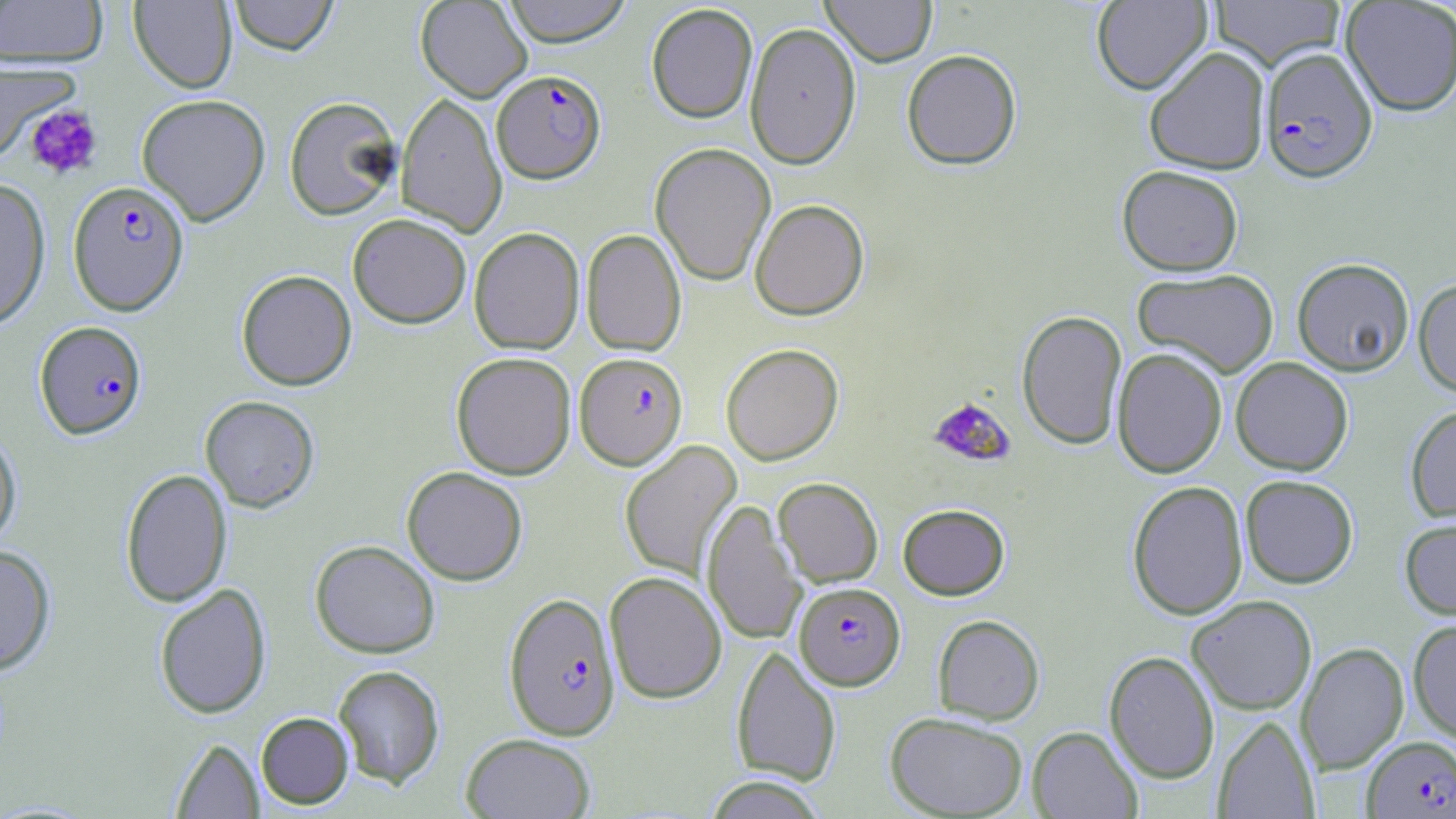
Approximate bounding boxes as (x1, y1, x2, y2) in pixels. Plasmodium falciparum-infected red blood cell locations: (1260, 47, 1378, 183), (492, 70, 606, 183), (67, 181, 189, 315), (34, 321, 147, 439), (577, 355, 690, 472), (795, 582, 905, 690), (503, 591, 621, 742), (1362, 735, 1456, 818). Uninfected red blood cell locations: (129, 0, 238, 94), (228, 0, 339, 56), (415, 0, 533, 102), (500, 0, 633, 46), (820, 0, 937, 67), (1091, 0, 1212, 95), (1341, 0, 1456, 116), (0, 1, 108, 68), (1210, 1, 1345, 71), (645, 3, 758, 124), (744, 22, 862, 169), (1143, 46, 1271, 175), (901, 50, 1022, 170), (0, 58, 80, 164), (395, 92, 507, 237), (136, 93, 271, 226), (284, 96, 402, 221), (650, 142, 776, 286), (1117, 165, 1243, 276), (0, 179, 51, 330), (750, 198, 869, 320), (348, 213, 472, 328), (468, 227, 585, 354), (581, 228, 686, 356), (1292, 257, 1414, 376), (1133, 268, 1279, 378), (236, 269, 357, 390), (1413, 277, 1456, 397), (1016, 309, 1127, 450), (720, 343, 844, 465), (1112, 347, 1228, 478), (451, 351, 577, 480), (1230, 357, 1353, 475), (200, 395, 320, 512), (1405, 404, 1456, 522), (0, 427, 22, 551), (619, 440, 742, 581), (402, 466, 528, 585), (120, 468, 232, 607), (1240, 474, 1358, 588), (773, 477, 883, 587), (1127, 480, 1248, 620), (702, 500, 806, 646), (898, 503, 1009, 600), (1399, 517, 1456, 620), (310, 540, 440, 659), (0, 545, 56, 675), (604, 571, 727, 704), (154, 583, 272, 718), (1187, 595, 1317, 714), (932, 614, 1044, 724), (1408, 619, 1456, 742), (1296, 642, 1408, 773), (732, 645, 841, 786), (1104, 650, 1220, 783), (333, 664, 445, 790), (256, 712, 354, 809), (885, 712, 1029, 818), (1213, 715, 1318, 818), (1027, 726, 1143, 818), (461, 733, 596, 818), (171, 737, 263, 818), (702, 775, 828, 818). Platelet locations: (24, 104, 103, 180), (928, 396, 1012, 466). Slide-level diagnosis: Plasmodium falciparum. Single field of view. Captured at 1000x magnification. May-Grünwald-Giemsa stain. Image is 1456×819 pixels. Thin blood film. Optical microscopy.